Classify this cell by malaria status.
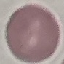

Uninfected.

capture = smartphone through the microscope eyepiece
stain = Giemsa
preparation = thin smear
image type = automatically extracted cell patch, resized to 64 × 64 pixels